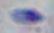
Summary:
  - Magnification: 1000x
  - Identification: Toxoplasma gondii
  - Modality: photomicrograph